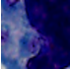

Summary:
  - Identification: leukocyte
  - Modality: photomicrograph
  - Magnification: 1000x